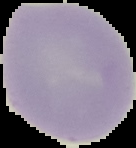
image type = cell region segmented out of the field of view; surrounding area masked to black
image size = 136×148 pixels
preparation = thin blood film
result = negative for Plasmodium parasites